Assess this cell for malaria.
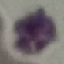

It is uninfected.

{
  "capture": "smartphone through the microscope eyepiece",
  "stain": "Giemsa",
  "image_type": "automatically extracted cell patch, resized to 64 × 64 pixels",
  "preparation": "thin blood film"
}